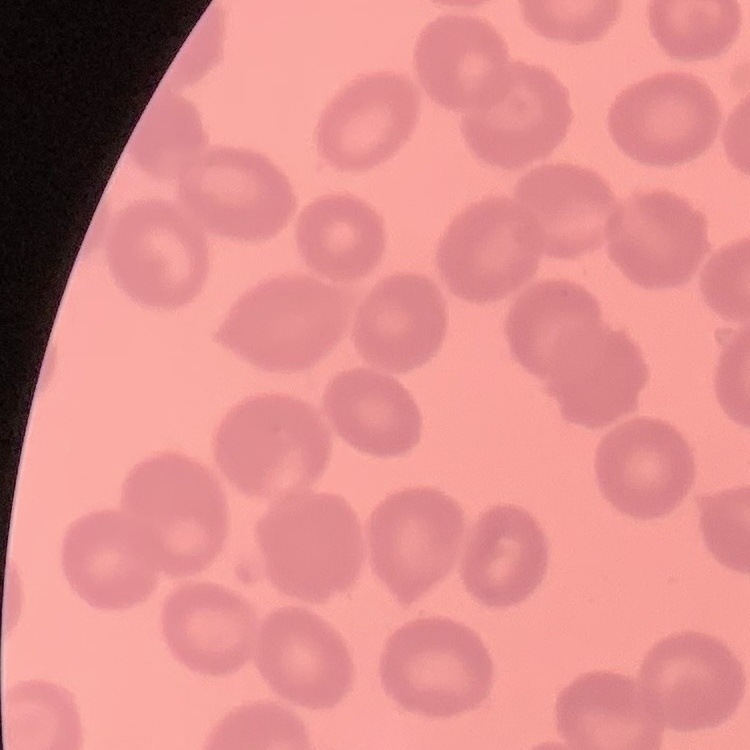

{
  "erythrocyte_morphology": "no rouleaux formation",
  "preparation": "thin blood film",
  "stain": "Field's or Giemsa",
  "image_type": "one tile cut from a larger photomicrograph"
}